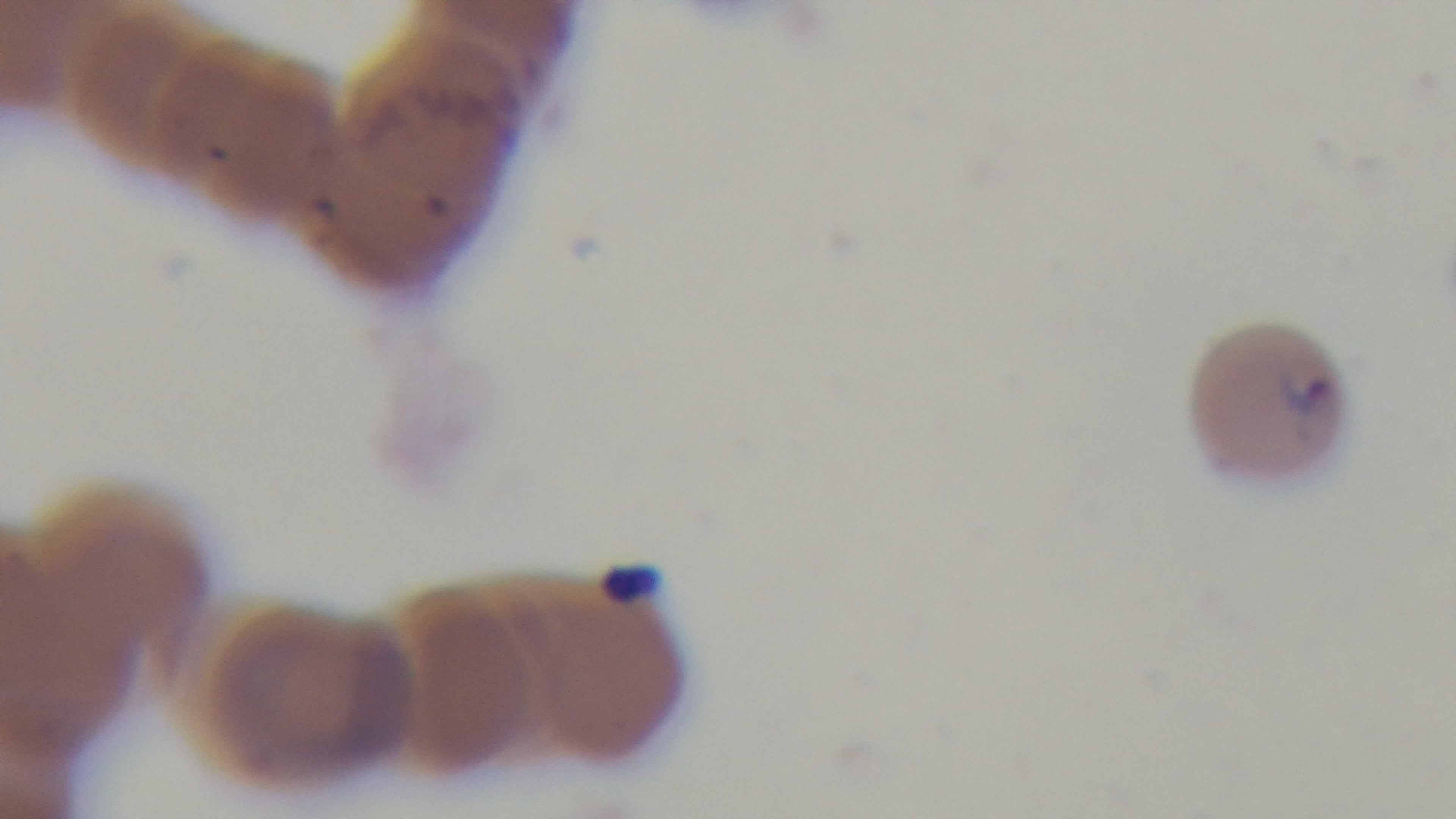
Summary:
  - Objective: 100x oil immersion
  - Preparation: thin blood film
  - Field of view: single
  - Malaria status: infected
  - Capture: mounted 4K digital camera
  - Modality: light microscopy
  - Stain: Giemsa